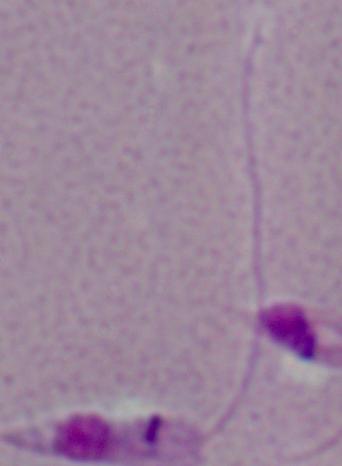

Summary:
  - Magnification: 1000x
  - Identification: Leishmania
  - Modality: photomicrograph